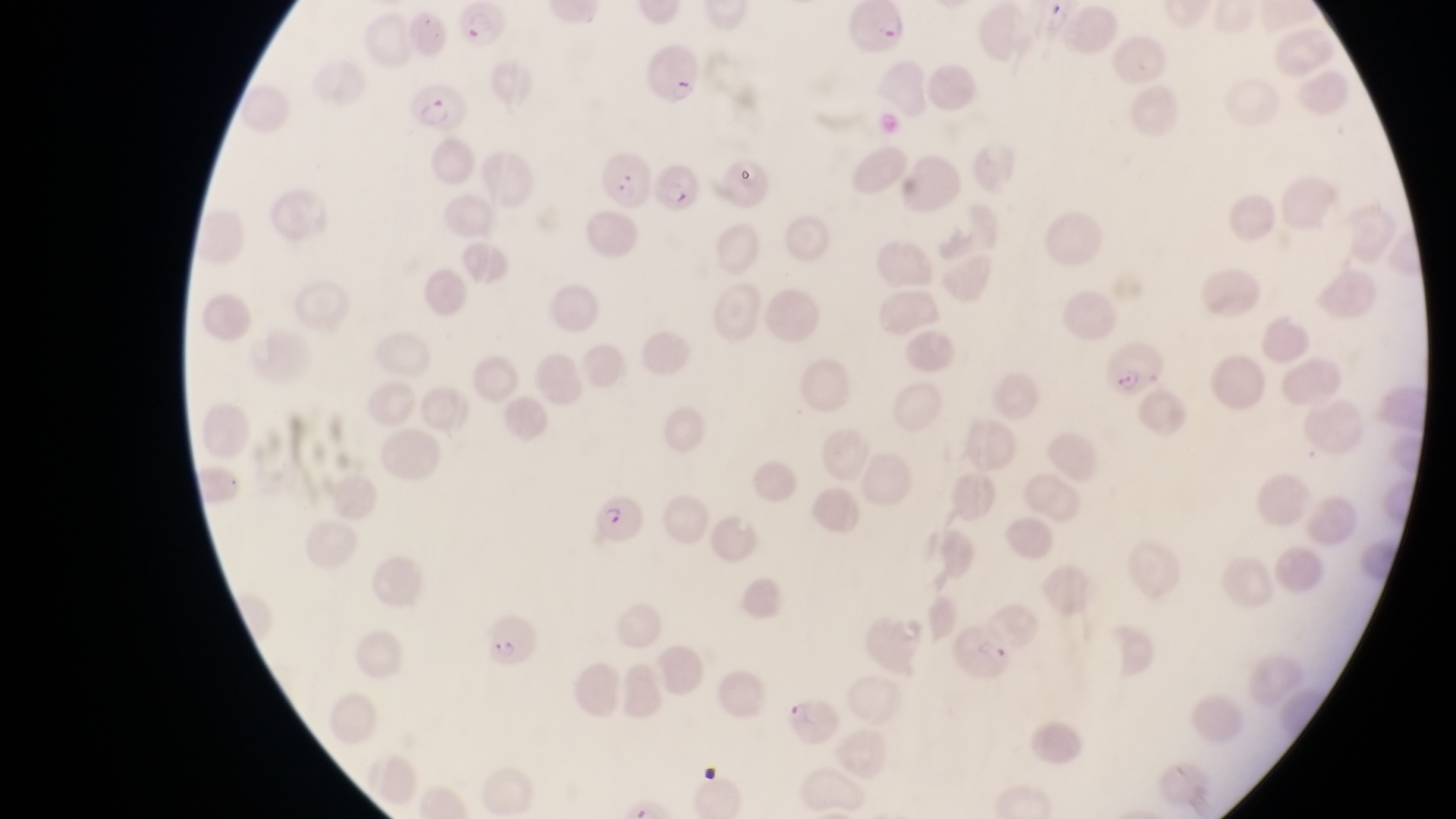
Approximate bounding boxes as (left, top, right, bottom) in pixels.
Summary:
  - Artifact (platelet-like body, stain precipitate, or debris) locations: (954, 618, 1018, 682)
  - Trophozoite locations: (1043, 2, 1076, 38)
  - Parasitised red blood cell locations: (848, 3, 911, 59), (457, 5, 513, 58), (647, 46, 707, 106), (410, 83, 470, 138), (594, 145, 657, 206), (653, 161, 708, 219), (1099, 334, 1166, 395), (587, 489, 643, 542), (481, 613, 545, 672), (789, 695, 844, 750)
  - Preparation: thin blood smear
  - Country: Uganda
  - Capture: smartphone photograph through the eyepiece of an Olympus CX-23 microscope
  - Magnification: 1000x
  - Field of view: single
  - Image size: 1456×819 pixels